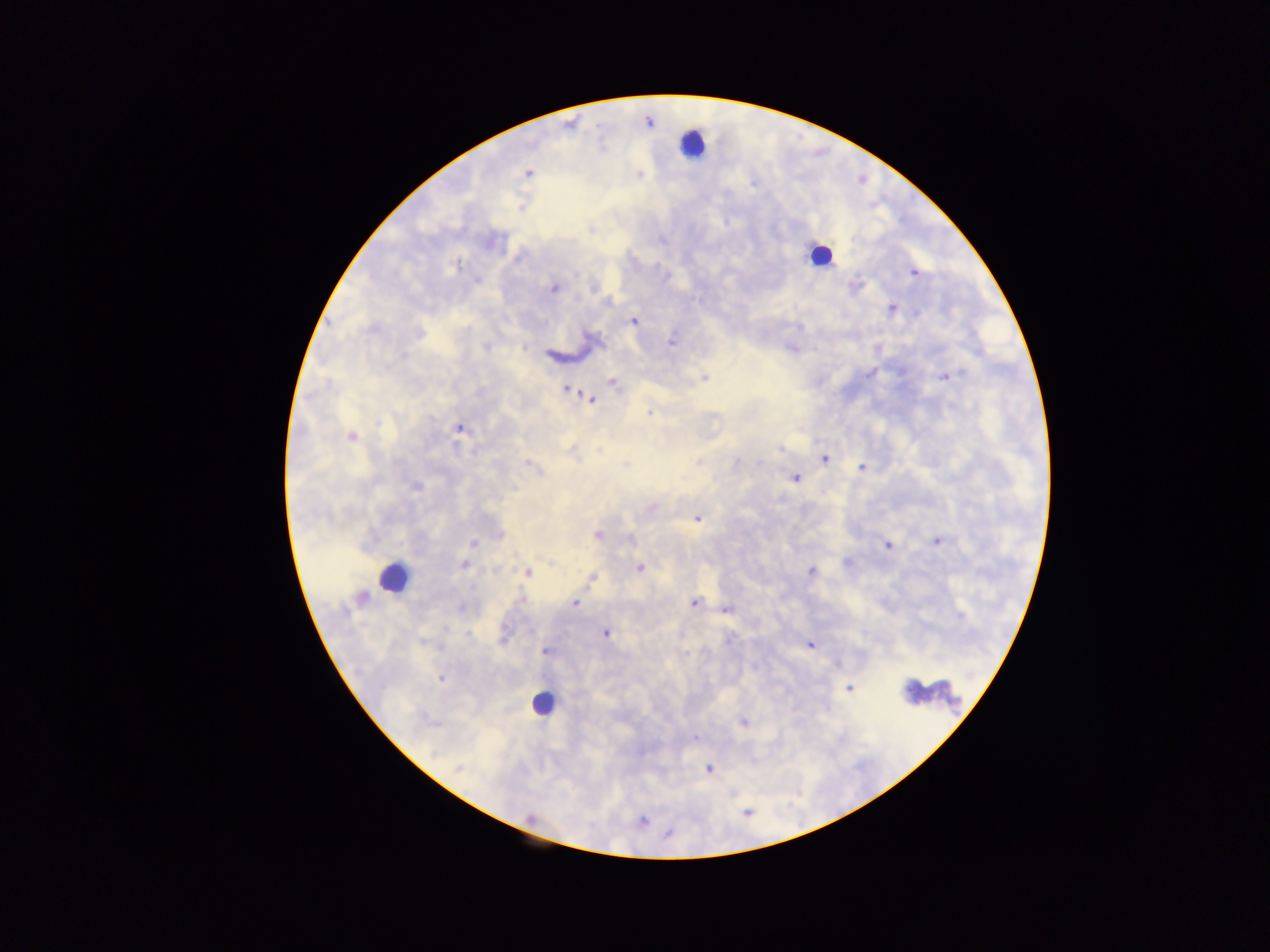

{
  "image_size": "1270×952 pixels",
  "capture": "mobile-phone photograph through a microscope",
  "country": "Ghana",
  "leukocyte_locations": "approximate centers as {x, y} in pixels: {691, 142}, {814, 254}, {392, 577}, {537, 705}",
  "plasmodium_parasite_locations": "approximate centers as {x, y} in pixels: {527, 171}, {751, 187}, {724, 223}, {914, 273}, {667, 277}, {477, 282}, {857, 285}, {553, 289}, {893, 308}, {634, 322}, {417, 331}, {672, 341}, {485, 346}, {524, 347}, {792, 347}, {402, 354}, {871, 373}, {705, 376}, {948, 376}, {614, 383}, {565, 389}, {591, 399}, {648, 411}, {457, 427}, {599, 448}, {780, 448}, {575, 458}, {824, 458}, {698, 461}, {738, 463}, {528, 464}, {625, 464}, {758, 464}, {862, 466}, {797, 479}, {417, 489}, {696, 519}, {597, 535}, {630, 540}, {940, 542}, {472, 543}, {888, 546}, {464, 567}, {640, 567}, {810, 571}, {528, 572}, {591, 578}, {522, 598}, {574, 603}, {694, 604}, {727, 610}, {467, 633}, {606, 633}, {505, 638}, {811, 644}, {543, 651}, {440, 679}, {850, 688}, {743, 722}, {696, 734}, {710, 767}, {459, 768}, {643, 820}, {669, 834}",
  "field_of_view": "single",
  "preparation": "thick blood smear"
}